Report the malaria status of this cell.
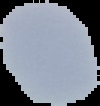
It is uninfected.

{
  "preparation": "thin blood smear",
  "image_type": "segmented cell region with the area outside set to black",
  "image_size": "100×106 pixels"
}